Locate every blood parasite and identify its species.
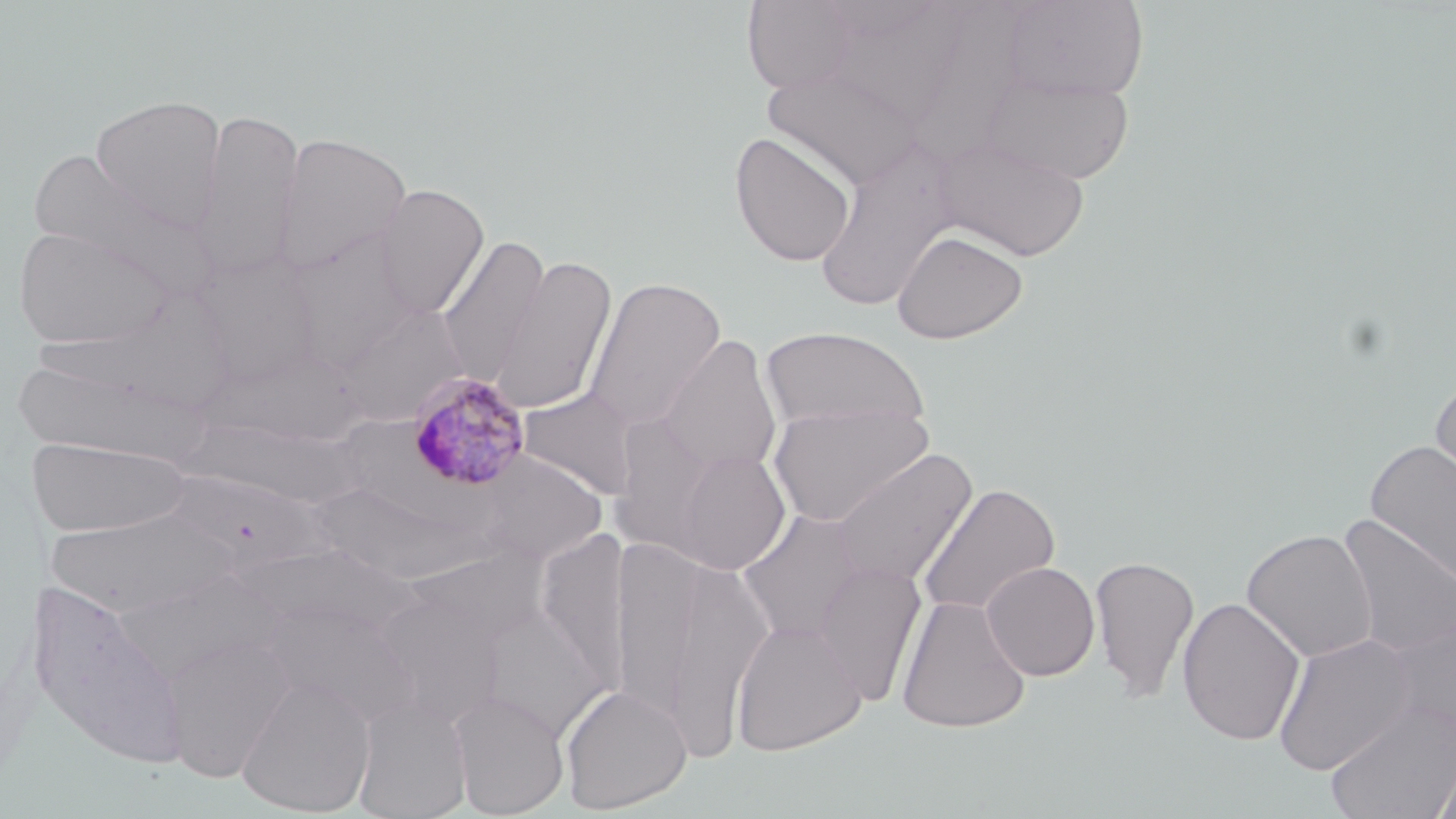

Approximate bounding boxes as [x1, y1, x2, y2] in pixels.
Plasmodium malariae-infected red blood cells: [404, 370, 533, 492].
No Plasmodium falciparum, Plasmodium ovale, Plasmodium vivax, Babesia divergens, or Trypanosoma brucei observed.

Uninfected red blood cell locations: [742, 0, 863, 94], [999, 0, 1149, 101], [818, 1, 974, 123], [763, 64, 925, 190], [980, 69, 1135, 185], [90, 94, 227, 232], [193, 107, 305, 281], [274, 131, 412, 277], [729, 131, 857, 267], [934, 135, 1090, 262], [812, 139, 962, 314], [24, 149, 209, 290], [374, 184, 489, 319], [13, 224, 177, 351], [281, 229, 423, 371], [892, 229, 1028, 344], [437, 233, 550, 387], [190, 254, 322, 387], [491, 256, 617, 415], [583, 276, 726, 431], [335, 303, 468, 425], [761, 326, 929, 436], [658, 335, 782, 479], [201, 347, 367, 446], [12, 352, 202, 465], [1428, 376, 1456, 503], [518, 389, 640, 498], [767, 401, 933, 528], [27, 437, 191, 538], [1364, 439, 1456, 587], [665, 448, 791, 576], [831, 448, 978, 590], [476, 452, 608, 565], [159, 470, 338, 575], [917, 483, 1060, 619], [318, 493, 509, 580], [44, 507, 236, 618], [736, 509, 870, 645], [1335, 512, 1456, 661], [1241, 528, 1378, 663], [227, 540, 429, 652], [616, 540, 773, 754], [1089, 555, 1200, 703], [813, 560, 927, 707], [981, 561, 1100, 681], [23, 578, 191, 769], [373, 585, 511, 728], [895, 594, 1032, 734], [1176, 596, 1306, 746], [258, 597, 421, 729], [475, 598, 613, 738], [1382, 615, 1456, 742], [729, 618, 866, 756], [158, 632, 296, 782], [1271, 632, 1419, 777], [236, 674, 377, 817], [560, 683, 692, 813], [448, 689, 569, 817], [353, 699, 473, 819], [1324, 699, 1456, 819], [1430, 747, 1456, 819]. Slide-level diagnosis: Plasmodium malariae. Thin blood smear. Light microscopy. One field of a larger specimen. May-Grünwald-Giemsa stain. 1000x magnification. Image is 1456×819 pixels.